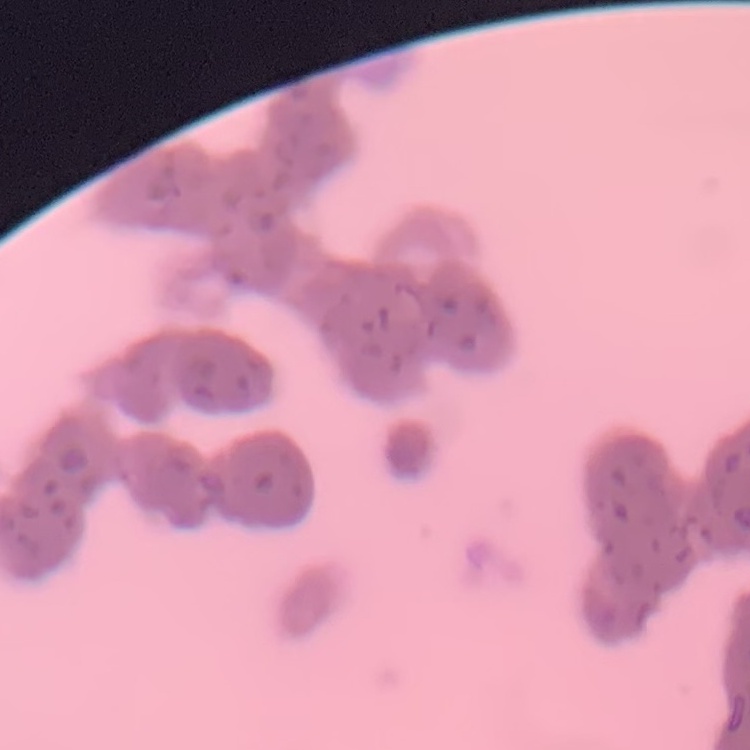

Summary:
  - Red blood cell morphology: rouleaux formation
  - Preparation: thin blood film
  - Stain: Field's or Giemsa
  - Image type: one tile cut from a larger photomicrograph